Give the location of every WBC.
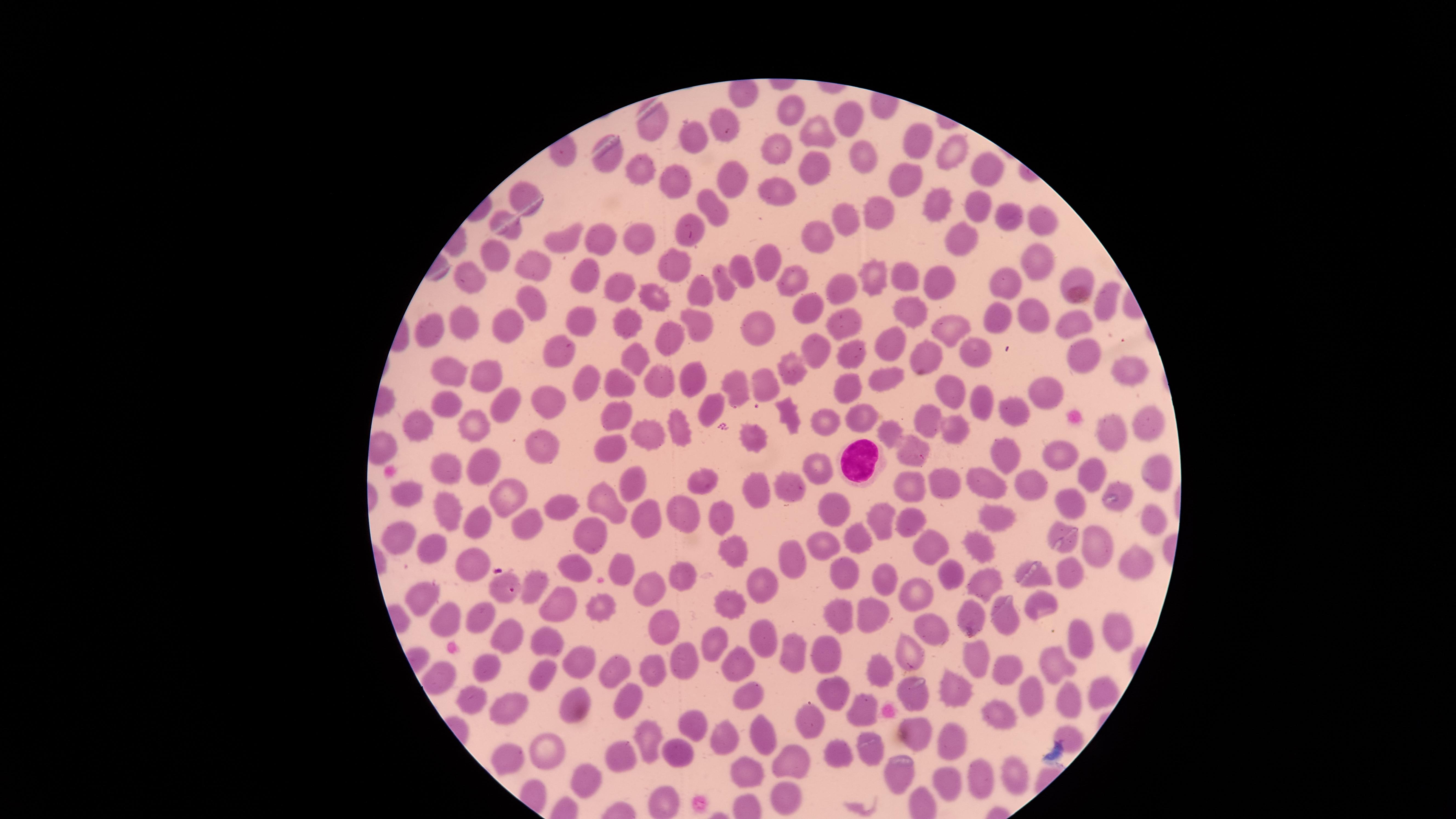

Approximate marker points, in pixels from the top-left corner.
WBCs: (x=860, y=460).

uninfected_RBCs: 'approximate marker points, in pixels from the top-left corner: (x=793, y=110), (x=842, y=118), (x=651, y=123), (x=727, y=124), (x=815, y=131), (x=909, y=136), (x=684, y=137), (x=775, y=144), (x=950, y=148), (x=866, y=155), (x=608, y=160), (x=983, y=166), (x=814, y=167), (x=637, y=170), (x=733, y=177), (x=677, y=181), (x=904, y=182), (x=773, y=191), (x=522, y=192), (x=975, y=202), (x=936, y=204), (x=710, y=205), (x=881, y=212), (x=843, y=214), (x=1004, y=216), (x=1034, y=217), (x=509, y=229), (x=693, y=233), (x=824, y=236), (x=598, y=238), (x=640, y=239), (x=956, y=239), (x=558, y=242), (x=499, y=256), (x=768, y=259), (x=1031, y=259), (x=530, y=264), (x=671, y=269), (x=735, y=269), (x=581, y=276), (x=904, y=276), (x=873, y=279), (x=939, y=279), (x=1071, y=279), (x=725, y=281), (x=469, y=283), (x=614, y=284), (x=798, y=284), (x=1008, y=285), (x=834, y=286), (x=702, y=292), (x=653, y=294), (x=528, y=301), (x=1109, y=306), (x=1031, y=309), (x=804, y=310), (x=905, y=310), (x=995, y=318), (x=621, y=320), (x=461, y=321), (x=842, y=321), (x=578, y=322), (x=695, y=322), (x=756, y=325), (x=1070, y=325), (x=942, y=330), (x=510, y=333), (x=430, y=334), (x=673, y=342), (x=817, y=344), (x=891, y=344), (x=969, y=346), (x=557, y=349), (x=633, y=352), (x=1082, y=354), (x=848, y=356), (x=925, y=362), (x=1121, y=367), (x=451, y=370), (x=488, y=371), (x=786, y=371), (x=880, y=375), (x=689, y=376), (x=580, y=379), (x=762, y=379), (x=656, y=382), (x=621, y=383), (x=1047, y=387), (x=848, y=389), (x=738, y=391), (x=953, y=395), (x=980, y=396), (x=506, y=397), (x=446, y=407), (x=546, y=408), (x=1012, y=409), (x=712, y=411), (x=856, y=411), (x=786, y=412), (x=611, y=413), (x=1152, y=417), (x=467, y=422), (x=823, y=423), (x=922, y=423), (x=420, y=425), (x=674, y=426), (x=645, y=430), (x=884, y=433), (x=949, y=435), (x=1118, y=436), (x=747, y=438), (x=542, y=444), (x=612, y=451), (x=910, y=451), (x=1054, y=458), (x=1004, y=461), (x=1145, y=461), (x=483, y=463), (x=813, y=463), (x=441, y=467), (x=1100, y=477), (x=943, y=483), (x=704, y=485), (x=908, y=486), (x=1030, y=486), (x=636, y=489), (x=793, y=489), (x=990, y=491), (x=760, y=492), (x=408, y=493), (x=509, y=495), (x=559, y=502), (x=1069, y=502), (x=614, y=503), (x=448, y=508), (x=838, y=509), (x=688, y=513), (x=1149, y=516), (x=994, y=518), (x=877, y=519), (x=651, y=520), (x=906, y=522), (x=484, y=523), (x=529, y=524), (x=717, y=525), (x=1059, y=532), (x=585, y=535), (x=402, y=537), (x=858, y=537), (x=823, y=544), (x=979, y=544), (x=438, y=546), (x=730, y=546), (x=1101, y=548), (x=930, y=551), (x=792, y=557), (x=579, y=561), (x=619, y=564), (x=478, y=566), (x=1138, y=566), (x=846, y=568), (x=1068, y=571), (x=684, y=573), (x=949, y=574), (x=1035, y=576), (x=881, y=580), (x=982, y=580), (x=765, y=586), (x=497, y=589), (x=537, y=589), (x=643, y=589), (x=917, y=595), (x=426, y=596), (x=600, y=597), (x=554, y=603), (x=736, y=603), (x=1042, y=604), (x=1005, y=609), (x=872, y=612), (x=967, y=613), (x=837, y=616), (x=449, y=620), (x=482, y=620), (x=1113, y=624), (x=931, y=625), (x=666, y=631), (x=512, y=635), (x=765, y=638), (x=1084, y=640), (x=545, y=641), (x=713, y=642), (x=791, y=651), (x=909, y=651), (x=582, y=653), (x=825, y=656), (x=484, y=660), (x=976, y=660), (x=680, y=661), (x=733, y=666), (x=1054, y=668), (x=1009, y=669), (x=609, y=671), (x=880, y=672), (x=536, y=674), (x=654, y=675), (x=441, y=676), (x=829, y=686), (x=1100, y=686), (x=955, y=689), (x=1027, y=693), (x=910, y=695), (x=475, y=696), (x=753, y=696), (x=1066, y=700), (x=625, y=703), (x=574, y=705), (x=857, y=709), (x=513, y=712), (x=689, y=717), (x=1001, y=717), (x=808, y=722), (x=913, y=724), (x=763, y=731), (x=645, y=733), (x=1068, y=734), (x=949, y=738), (x=724, y=739), (x=546, y=748), (x=869, y=748), (x=842, y=752), (x=626, y=756), (x=678, y=756), (x=790, y=756), (x=511, y=758), (x=742, y=770), (x=1017, y=772), (x=897, y=776), (x=976, y=777), (x=590, y=781), (x=946, y=787), (x=781, y=795), (x=662, y=803)'
presence: no malaria parasites identified
capture: smartphone photograph through the microscope eyepiece
preparation: thin blood smear
field_of_view: single
stain: Giemsa
visible_region: circular
image_size: 1456×819 pixels